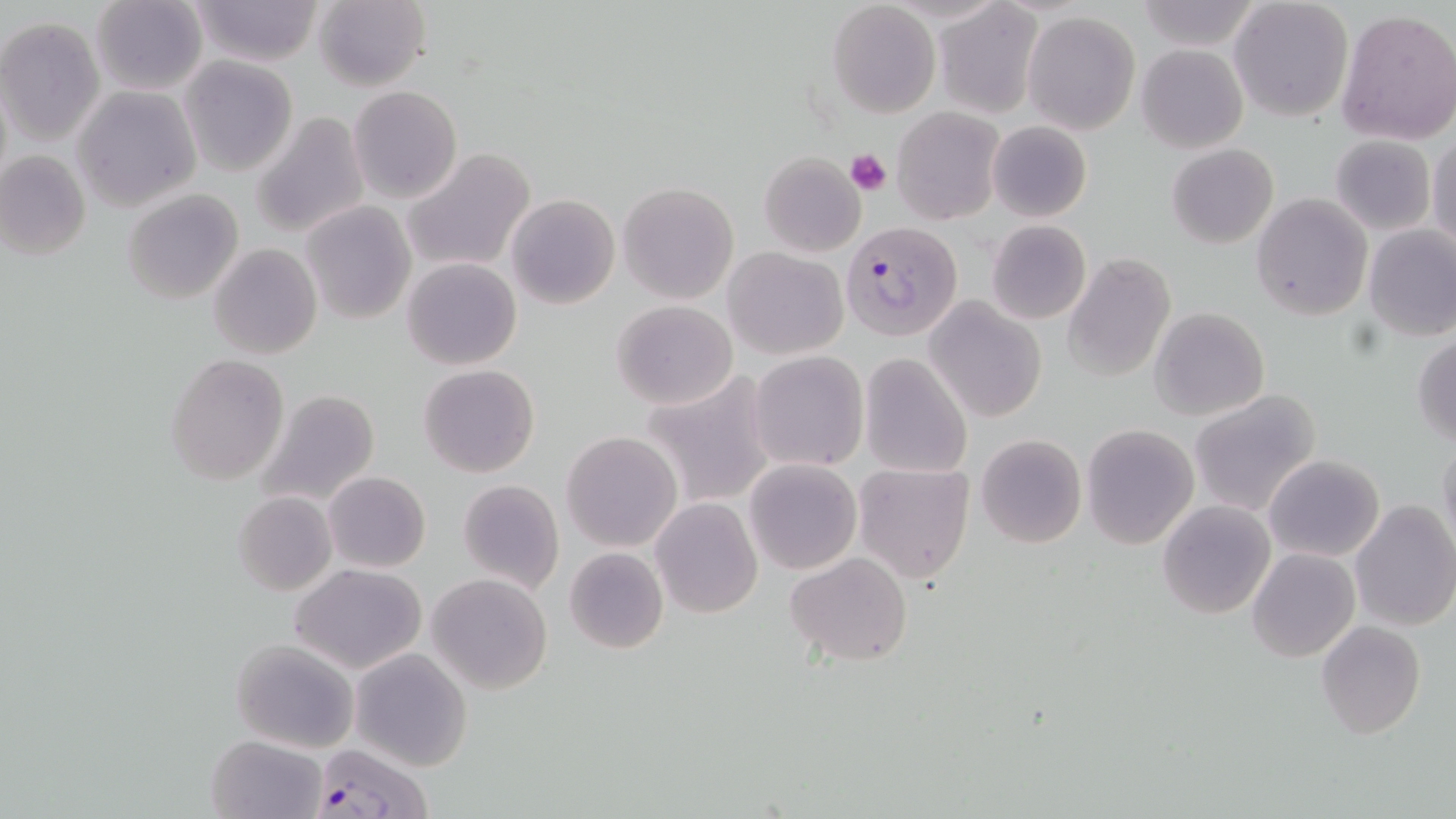
Summary:
  - Coordinate format: approximate bounding boxes as [x1, y1, x2, y2] in pixels
  - Platelet locations: [846, 148, 892, 195]
  - Plasmodium falciparum-infected red blood cell locations: [842, 220, 964, 340], [310, 741, 434, 819]
  - Uninfected red blood cell locations: [91, 0, 208, 96], [186, 0, 326, 68], [313, 0, 430, 90], [1230, 0, 1354, 122], [1133, 1, 1260, 49], [827, 3, 940, 117], [935, 3, 1042, 116], [1335, 8, 1456, 145], [1023, 11, 1139, 134], [1, 17, 104, 145], [1136, 44, 1248, 152], [179, 57, 298, 176], [349, 85, 462, 204], [73, 86, 201, 211], [893, 106, 1003, 225], [252, 110, 371, 238], [987, 120, 1092, 222], [1331, 135, 1436, 235], [1428, 135, 1456, 252], [1167, 144, 1279, 249], [401, 148, 536, 275], [0, 149, 91, 260], [758, 152, 865, 257], [617, 180, 739, 305], [121, 189, 243, 305], [1252, 192, 1373, 321], [505, 193, 620, 310], [300, 202, 415, 326], [986, 219, 1091, 325], [1364, 224, 1456, 342], [207, 244, 322, 362], [724, 248, 848, 359], [1064, 253, 1176, 384], [402, 258, 522, 370], [925, 297, 1047, 424], [613, 300, 737, 410], [1150, 307, 1270, 420], [1412, 333, 1456, 445], [749, 351, 870, 473], [165, 353, 289, 484], [858, 353, 973, 479], [419, 365, 540, 479], [640, 370, 779, 511], [1189, 389, 1322, 516], [258, 390, 381, 510], [1081, 424, 1198, 548], [562, 430, 682, 551], [975, 434, 1087, 548], [1438, 438, 1456, 557], [1264, 453, 1384, 563], [744, 459, 861, 574], [852, 461, 975, 582], [323, 472, 430, 573], [457, 479, 565, 593], [232, 491, 337, 596], [651, 498, 761, 618], [1350, 499, 1456, 632], [1157, 501, 1275, 620], [562, 546, 669, 655], [1247, 548, 1359, 661], [784, 552, 913, 664], [289, 563, 426, 674], [427, 572, 551, 695], [1316, 620, 1426, 738], [230, 638, 361, 754], [351, 649, 472, 770], [206, 735, 325, 818]
  - Slide-level diagnosis: Plasmodium falciparum
  - Magnification: 1000x
  - Modality: light microscopy
  - Field of view: one of a larger specimen
  - Preparation: thin blood smear
  - Image size: 1456×819 pixels
  - Stain: May-Grünwald-Giemsa